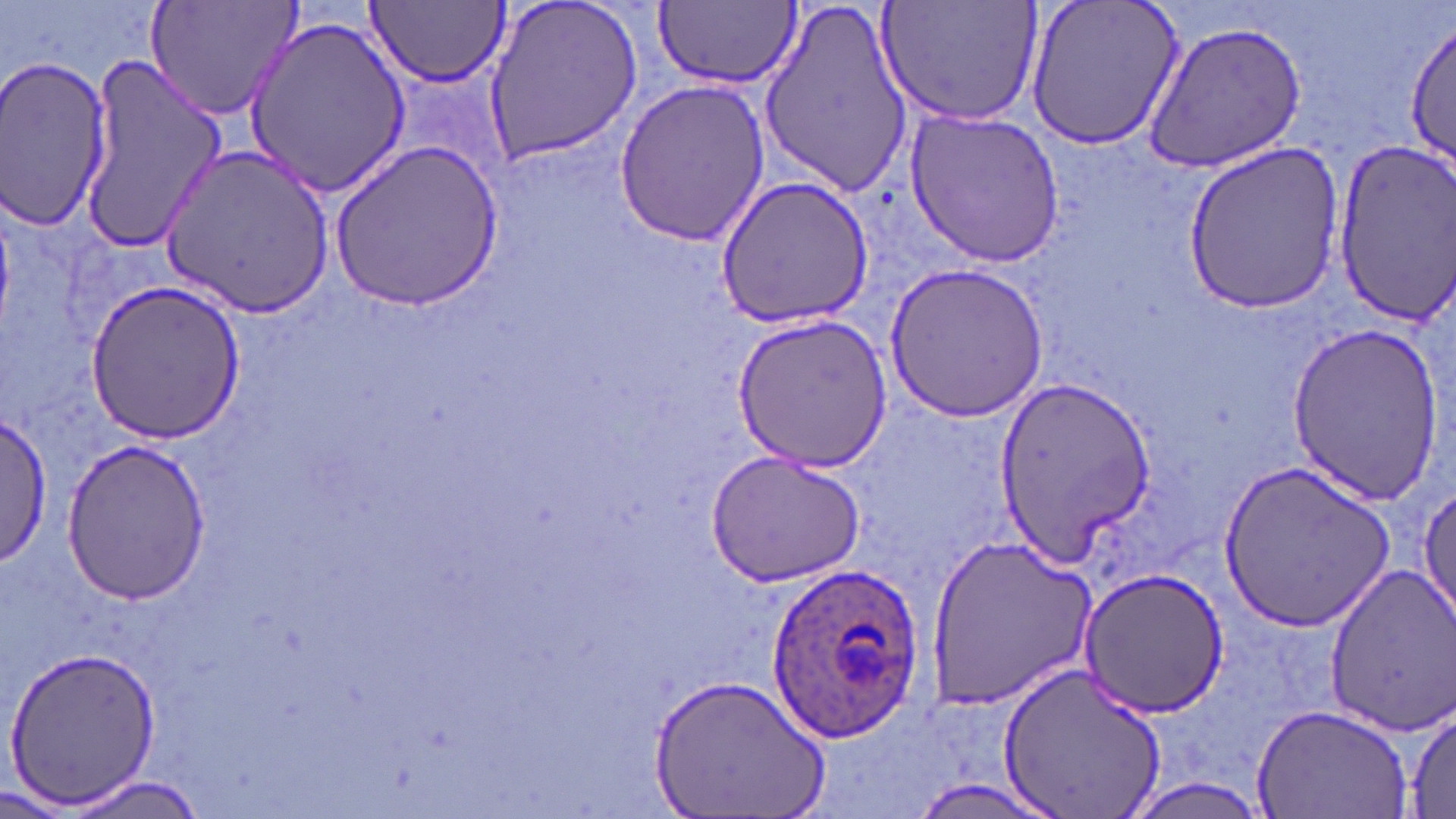

Approximate bounding boxes as (x1, y1, x2, y2) in pixels. Uninfected red blood cell locations: (147, 0, 304, 121), (481, 0, 643, 165), (757, 0, 915, 198), (877, 0, 1044, 128), (1025, 0, 1186, 152), (364, 1, 510, 90), (651, 1, 802, 91), (243, 13, 411, 199), (1405, 17, 1455, 174), (1142, 22, 1310, 171), (77, 46, 225, 251), (0, 57, 116, 233), (614, 77, 771, 248), (905, 107, 1064, 265), (330, 139, 503, 309), (1177, 143, 1350, 315), (1331, 144, 1456, 321), (161, 146, 334, 317), (715, 175, 875, 329), (883, 262, 1048, 423), (85, 279, 246, 445), (733, 315, 892, 471), (1284, 320, 1444, 505), (995, 374, 1154, 566), (0, 414, 52, 568), (59, 441, 215, 605), (704, 451, 866, 587), (1218, 459, 1397, 630), (1413, 481, 1455, 629), (925, 535, 1100, 707), (1076, 564, 1229, 717), (1325, 565, 1456, 734), (5, 644, 163, 808), (995, 658, 1170, 819), (651, 673, 831, 819), (1252, 701, 1414, 818), (1405, 701, 1456, 817), (64, 772, 212, 818), (0, 782, 79, 817). Plasmodium ovale-infected red blood cell locations: (765, 558, 928, 741). Slide-level diagnosis: Plasmodium ovale. May-Grünwald-Giemsa stain. Optical microscopy. Thin blood smear. Captured at 1000x magnification. Single field of view. Image is 1456×819 pixels.